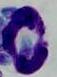

modality = photomicrograph
identification = leukocyte
magnification = 1000x